Give the position of every leukocyte.
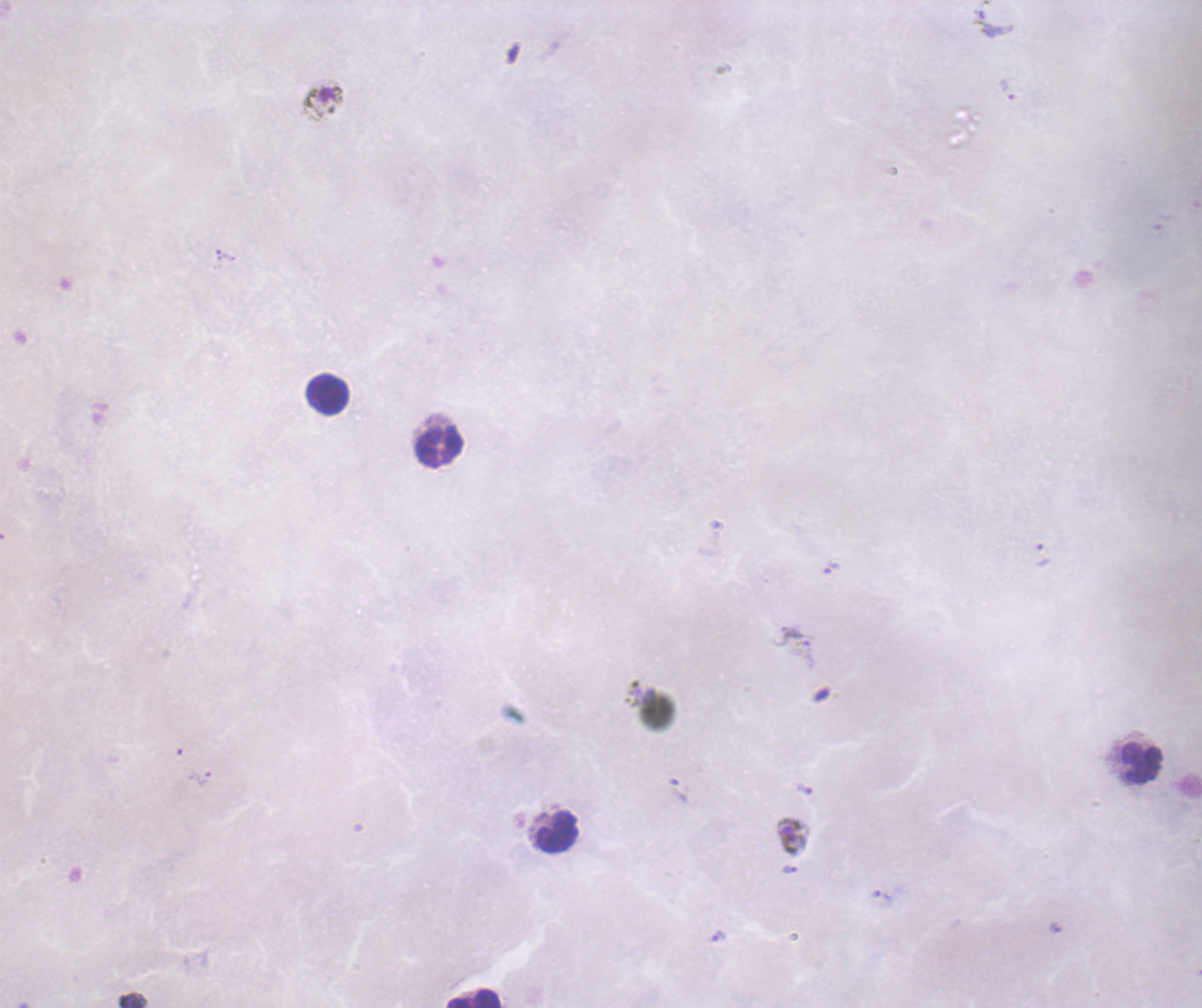

Approximate object centers, in pixels from the top-left corner.
Leukocytes: (x=327, y=395), (x=438, y=445), (x=1140, y=763), (x=555, y=832), (x=475, y=997).

Approximate object centers, in pixels from the top-left corner.
Summary:
  - Gametocyte locations: (x=322, y=103), (x=791, y=835)
  - Trophozoite locations: (x=830, y=567), (x=199, y=778), (x=805, y=789), (x=789, y=869), (x=719, y=936)
  - Life-cycle stages observed: trophozoite, gametocyte
  - Result: malaria parasites identified
  - Magnification: 100x
  - Preparation: thick blood smear
  - Stain: Romanowsky
  - Background quality: poor
  - Coloration quality: bad
  - Image size: 1202×1008 pixels
  - Context: previously used in an actual diagnosis
  - Field of view: one from this slide